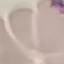

malaria status = uninfected
stain = Giemsa
preparation = thin blood smear
capture = smartphone camera at the microscope eyepiece
image type = cell patch, automatically extracted from a larger field of view and resized to 64 × 64 pixels